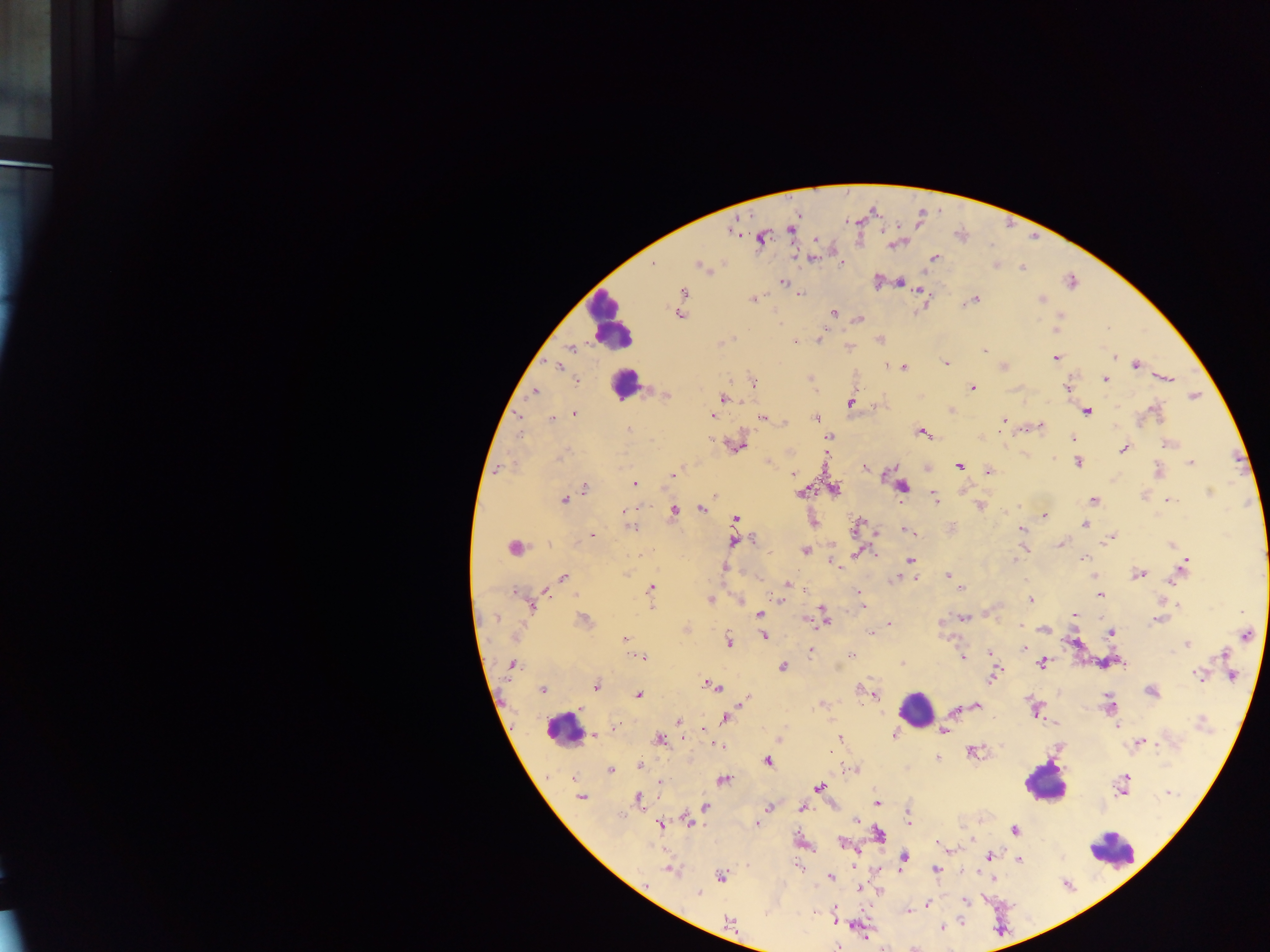

Approximate centers as {x, y} in pixels.
Summary:
  - Plasmodium parasite locations: {732, 230}, {791, 231}, {760, 238}, {816, 240}, {815, 257}, {934, 257}, {653, 263}, {842, 263}, {699, 266}, {1022, 268}, {876, 281}, {900, 282}, {782, 283}, {920, 291}, {684, 293}, {800, 294}, {751, 300}, {975, 300}, {1041, 300}, {834, 313}, {678, 315}, {1059, 316}, {859, 319}, {820, 338}, {879, 339}, {795, 342}, {571, 348}, {985, 350}, {1113, 357}, {1055, 358}, {946, 364}, {1135, 365}, {1004, 366}, {558, 367}, {903, 367}, {1168, 378}, {578, 380}, {1105, 380}, {753, 383}, {972, 388}, {1067, 388}, {535, 391}, {665, 396}, {1194, 396}, {724, 399}, {850, 403}, {1155, 410}, {1086, 412}, {574, 413}, {713, 415}, {519, 417}, {551, 418}, {761, 418}, {815, 418}, {1003, 420}, {784, 422}, {1039, 427}, {629, 430}, {922, 432}, {521, 435}, {828, 436}, {1073, 438}, {709, 440}, {1167, 444}, {738, 446}, {1123, 449}, {561, 457}, {1053, 459}, {1078, 463}, {1191, 463}, {959, 466}, {865, 467}, {499, 469}, {989, 472}, {1157, 472}, {673, 474}, {792, 475}, {635, 484}, {903, 487}, {585, 488}, {835, 489}, {801, 492}, {1210, 493}, {935, 498}, {564, 500}, {1093, 500}, {1172, 501}, {980, 507}, {636, 509}, {701, 509}, {628, 510}, {674, 511}, {1045, 516}, {736, 519}, {859, 523}, {1083, 524}, {630, 527}, {1021, 530}, {906, 531}, {591, 536}, {1111, 537}, {752, 540}, {735, 541}, {1060, 544}, {1171, 545}, {514, 547}, {805, 550}, {858, 553}, {1083, 558}, {909, 560}, {1015, 560}, {1185, 563}, {836, 564}, {725, 568}, {1139, 573}, {948, 575}, {563, 578}, {897, 578}, {915, 578}, {1173, 580}, {787, 585}, {650, 588}, {961, 588}, {805, 589}, {516, 592}, {544, 592}, {860, 593}, {1099, 595}, {710, 600}, {740, 600}, {781, 600}, {1031, 600}, {861, 605}, {1178, 605}, {531, 607}, {760, 614}, {824, 614}, {1075, 616}, {963, 617}, {496, 618}, {584, 620}, {806, 620}, {1157, 620}, {825, 621}, {890, 624}, {1020, 625}, {1045, 630}, {871, 632}, {1111, 633}, {1246, 636}, {763, 637}, {626, 639}, {729, 641}, {1187, 644}, {1025, 649}, {811, 653}, {990, 653}, {1223, 654}, {852, 655}, {641, 657}, {962, 657}, {1042, 663}, {512, 664}, {902, 664}, {782, 667}, {1198, 675}, {1232, 675}, {993, 677}, {713, 686}, {596, 687}, {861, 689}, {542, 690}, {1151, 691}, {874, 694}, {639, 695}, {744, 701}, {1109, 705}, {976, 706}, {955, 710}, {1035, 711}, {726, 719}, {678, 721}, {1115, 722}, {1202, 722}, {1117, 727}, {614, 729}, {943, 731}, {894, 734}, {594, 735}, {840, 738}, {683, 739}, {779, 739}, {661, 740}, {1141, 743}, {717, 746}, {973, 752}, {937, 757}, {768, 762}, {641, 765}, {854, 769}, {610, 770}, {723, 780}, {661, 783}, {1122, 784}, {819, 786}, {1168, 793}, {581, 797}, {639, 798}, {876, 802}, {705, 807}, {767, 807}, {802, 809}, {907, 814}, {857, 819}, {689, 822}, {757, 824}, {660, 825}, {1014, 830}, {879, 834}, {843, 844}, {941, 845}, {990, 856}, {904, 859}, {1020, 860}, {798, 867}, {936, 869}, {672, 871}, {721, 876}, {830, 876}, {992, 877}, {862, 888}, {699, 894}, {965, 901}, {927, 905}, {835, 909}, {908, 910}, {835, 920}, {730, 923}, {941, 927}, {838, 946}
  - Leukocyte locations: {610, 322}, {624, 384}, {915, 710}, {561, 731}, {1045, 783}, {1112, 851}
  - Image size: 1270×952 pixels
  - Capture: mobile-phone photograph through a microscope
  - Field of view: single
  - Preparation: thick blood smear
  - Country: Ghana